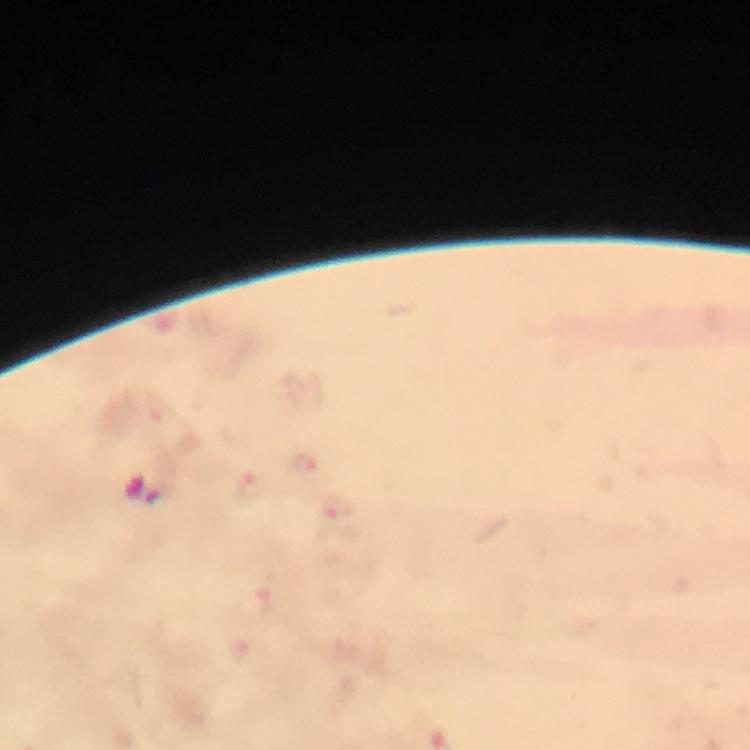
malaria parasite locations = approximate centers as (x, y) in pixels: (304, 465), (247, 489), (337, 511), (240, 654)
cropped from = one field of view
magnification = 100x
image size = 750×750 pixels
immersion oil = applied
context = from a malaria diagnostic workup
stain = Giemsa
capture = smartphone camera through the microscope
preparation = thick blood smear